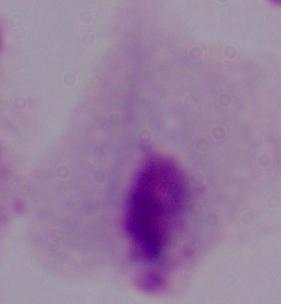
Photomicrograph. Captured at 1000x magnification. A trichomonad is shown.